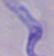
identification: trypanosome
magnification: 1000x
modality: photomicrograph